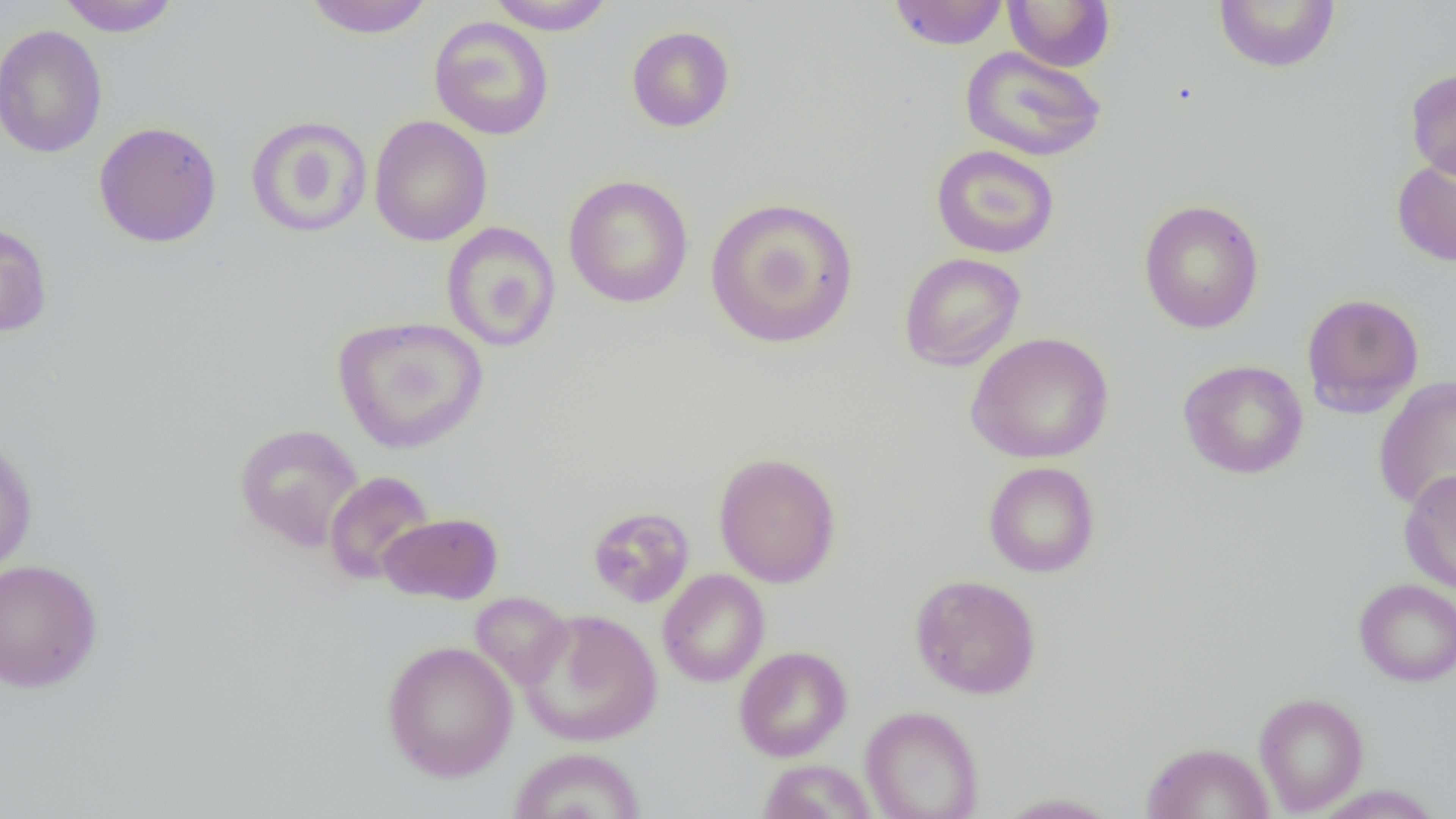
Summary:
  - Coordinate format: approximate bounding boxes as (x1, y1, x2, y2) in pixels
  - Uninfected red blood cell locations: (58, 0, 181, 37), (303, 0, 436, 38), (487, 0, 615, 34), (888, 0, 1009, 50), (1003, 0, 1116, 72), (1213, 0, 1341, 73), (429, 17, 554, 141), (0, 24, 108, 159), (627, 26, 734, 132), (960, 46, 1106, 162), (1405, 67, 1456, 181), (246, 115, 372, 238), (369, 115, 492, 246), (93, 120, 223, 248), (931, 145, 1060, 259), (1391, 154, 1456, 268), (563, 175, 693, 308), (705, 197, 859, 348), (1138, 199, 1265, 334), (0, 219, 53, 338), (441, 222, 561, 352), (898, 252, 1026, 371), (1302, 292, 1424, 417), (333, 316, 488, 454), (965, 332, 1115, 464), (1177, 359, 1309, 480), (1373, 375, 1456, 512), (234, 423, 364, 552), (0, 434, 38, 576), (713, 452, 842, 588), (983, 461, 1100, 578), (1398, 468, 1456, 594), (323, 470, 436, 586), (587, 506, 695, 607), (378, 512, 503, 604), (0, 557, 103, 693), (657, 569, 770, 687), (909, 574, 1042, 699), (1353, 579, 1456, 686), (470, 591, 573, 689), (519, 609, 662, 747), (381, 640, 518, 783), (734, 646, 852, 762), (1254, 692, 1369, 815), (860, 705, 984, 819), (1140, 741, 1275, 819), (508, 746, 646, 819), (757, 759, 878, 819), (992, 792, 1124, 818)
  - Slide-level diagnosis: no evidence of blood parasites
  - Preparation: thin blood film
  - Modality: optical microscopy
  - Image size: 1456×819 pixels
  - Field of view: one of a larger specimen
  - Magnification: 1000x